Comment on the morphology of the erythrocytes.
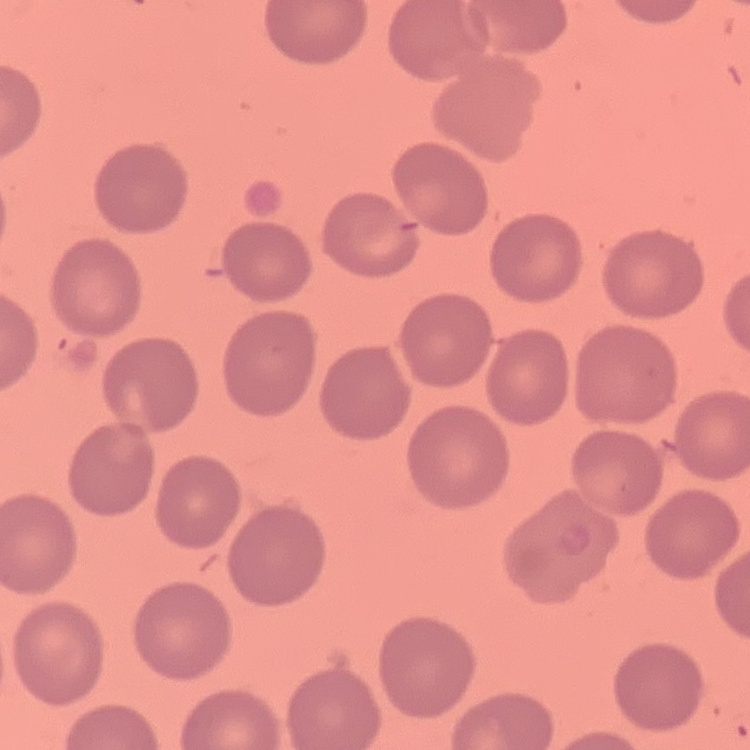
No rouleaux formation.

Summary:
  - Image type: one tile cut from a larger photomicrograph
  - Stain: Field's or Giemsa
  - Preparation: thin blood film